Report the malaria status of this cell.
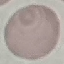

It is uninfected.

Summary:
  - Preparation: thin smear
  - Image type: automatically extracted cell patch, resized to 64 × 64 pixels
  - Stain: Giemsa
  - Capture: smartphone camera at the microscope eyepiece